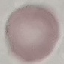

Summary:
  - Malaria status: uninfected
  - Image type: automatically extracted cell patch, resized to 64 × 64 pixels
  - Capture: smartphone through the microscope eyepiece
  - Stain: Giemsa
  - Preparation: thin blood film